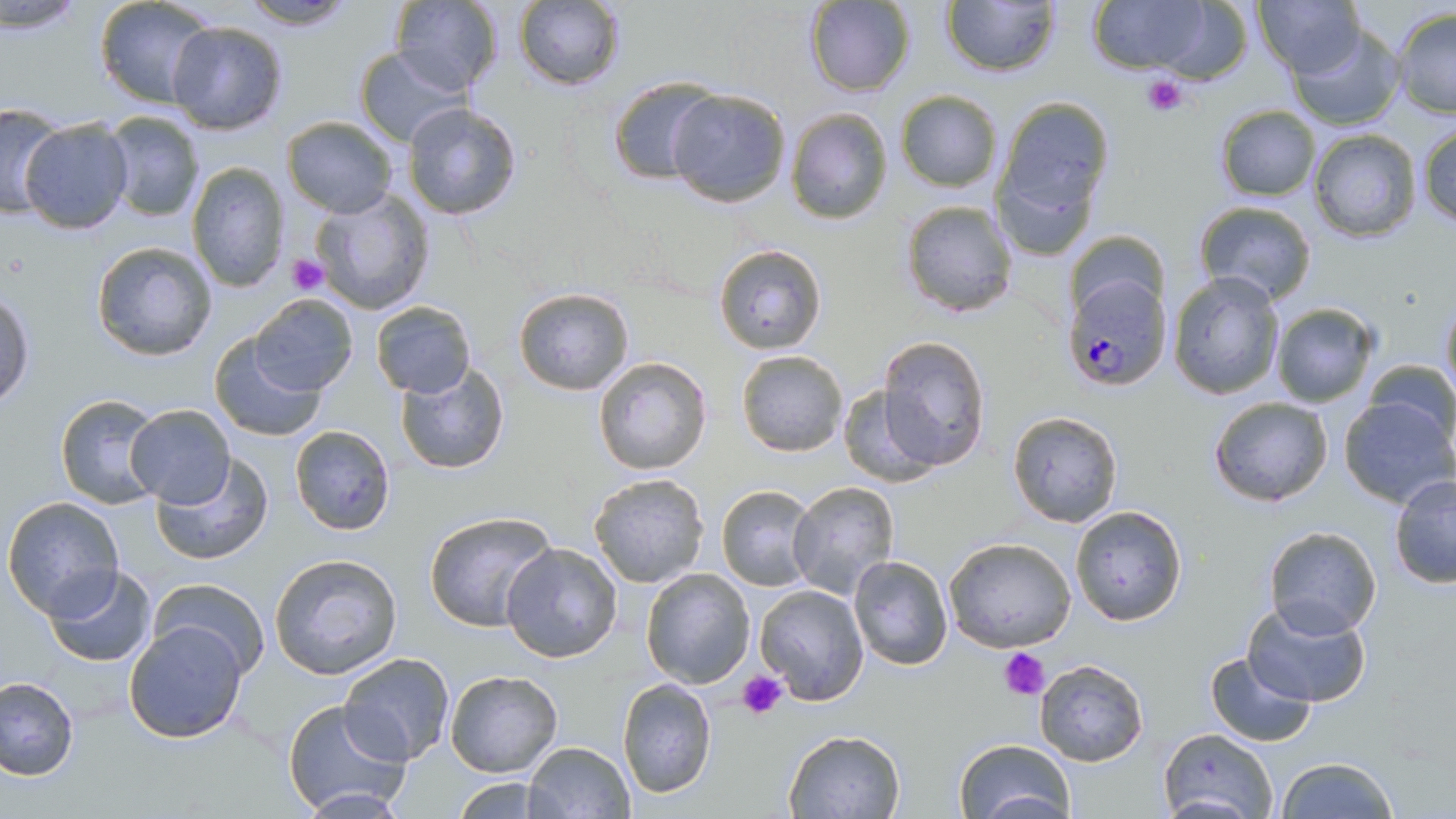

slide-level diagnosis = Plasmodium falciparum
modality = optical microscopy
platelet locations = approximate bounding boxes as (x1,y1)-(x2,y2) corner pairs in pixels: (1139,73)-(1192,118), (288,255)-(328,296), (998,646)-(1049,700), (739,670)-(790,720)
field of view = one of a larger specimen
stain = May-Grünwald-Giemsa
magnification = 1000x
image size = 1456×819 pixels
Plasmodium falciparum-infected red blood cell locations = approximate bounding boxes as (x1,y1)-(x2,y2) corner pairs in pixels: (1062,273)-(1172,392)
preparation = thin blood smear
uninfected red blood cell locations = approximate bounding boxes as (x1,y1)-(x2,y2) corner pairs in pixels: (95,0)-(218,108), (237,0)-(359,30), (942,0)-(1060,76), (1253,0)-(1366,79), (462,1)-(506,96), (513,1)-(627,91), (804,1)-(916,95), (1086,1)-(1220,76), (391,2)-(470,93), (0,3)-(91,36), (1149,5)-(1255,87), (1390,7)-(1455,121), (166,20)-(289,134), (1286,24)-(1406,130), (353,46)-(465,147), (609,76)-(721,185), (666,88)-(791,207), (895,90)-(1002,191), (992,95)-(1114,245), (403,99)-(522,219), (0,103)-(68,218), (1214,104)-(1321,201), (784,106)-(893,225), (101,110)-(206,222), (281,115)-(398,218), (16,117)-(135,234), (1416,120)-(1456,231), (1308,128)-(1422,243), (186,162)-(290,291), (309,189)-(435,314), (899,200)-(1018,317), (1193,201)-(1319,306), (1065,227)-(1168,319), (90,239)-(220,362), (713,244)-(826,355), (1167,271)-(1285,400), (514,288)-(635,396), (1,289)-(35,408), (249,292)-(358,396), (1438,296)-(1456,409), (370,300)-(475,398), (1269,301)-(1379,407), (208,331)-(328,441), (878,335)-(991,471), (735,350)-(848,457), (591,355)-(712,476), (1362,359)-(1456,450), (393,361)-(509,475), (836,383)-(941,486), (53,392)-(167,510), (1207,395)-(1334,507), (1337,395)-(1455,509), (123,404)-(235,509), (1006,411)-(1124,528), (289,425)-(396,535), (151,453)-(274,568), (587,472)-(710,589), (1389,474)-(1456,589), (787,482)-(899,601), (715,484)-(819,592), (3,496)-(125,618), (1068,504)-(1187,628), (424,509)-(557,632), (1263,526)-(1381,638), (942,537)-(1077,654), (500,541)-(623,663), (268,553)-(404,680), (847,555)-(954,672), (42,566)-(159,668), (640,567)-(756,687), (149,578)-(271,679), (753,583)-(869,704), (1241,599)-(1372,708), (124,622)-(247,744), (1204,650)-(1316,748), (337,653)-(455,767), (1032,659)-(1149,767), (445,671)-(563,777), (0,676)-(79,780), (615,678)-(717,800), (281,698)-(413,817), (784,728)-(907,818), (1158,728)-(1278,818), (953,738)-(1076,817), (523,741)-(634,819), (1275,757)-(1402,819), (451,777)-(551,817)